Locate and identify every blood parasite.
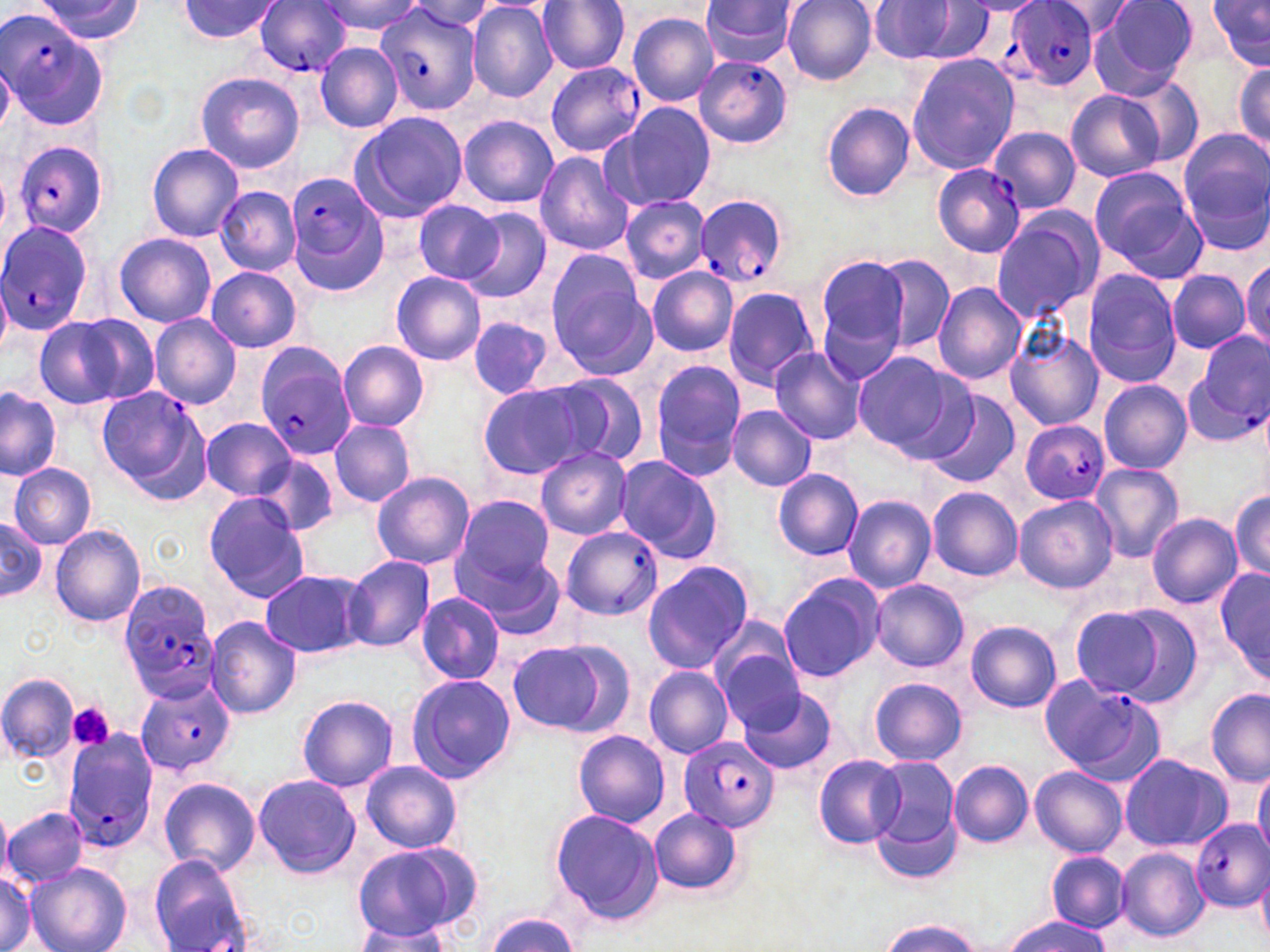

Approximate bounding boxes as (x1,y1)-(x2,y2) corner pairs in pixels.
Plasmodium falciparum-infected red blood cells (subset): (1010,0)-(1100,91), (253,2)-(353,76), (374,4)-(482,116), (0,8)-(103,130), (694,55)-(792,148), (545,61)-(644,156), (13,140)-(107,239), (933,163)-(1026,258), (285,172)-(387,288), (692,191)-(788,290), (0,217)-(95,336), (1194,333)-(1270,427), (257,352)-(359,461), (96,386)-(206,494), (1018,421)-(1109,504), (558,525)-(663,621), (1040,675)-(1163,780), (135,681)-(230,775), (62,731)-(159,854), (679,735)-(779,833), (1190,821)-(1270,912).
No Plasmodium ovale, Plasmodium malariae, Plasmodium vivax, Babesia divergens, or Trypanosoma brucei observed.

Summary:
  - Uninfected red blood cell locations (subset): (320,0)-(421,38), (700,0)-(801,65), (782,0)-(878,85), (1091,0)-(1198,94), (1209,0)-(1270,70), (35,1)-(142,44), (176,1)-(281,44), (405,1)-(499,35), (536,1)-(629,74), (1045,1)-(1139,38), (870,2)-(991,64), (468,3)-(559,102), (627,11)-(720,105), (314,42)-(404,132), (906,54)-(1020,175), (1232,54)-(1270,157), (0,60)-(14,138), (194,72)-(305,173), (1119,77)-(1203,164), (1065,89)-(1166,182), (821,101)-(915,201), (607,103)-(716,211), (348,111)-(468,224), (458,116)-(559,208), (987,126)-(1082,215), (1178,129)-(1270,236), (147,143)-(244,243), (533,151)-(633,256), (1087,165)-(1200,271), (216,187)-(300,277), (619,195)-(709,284), (412,199)-(504,285), (459,207)-(553,304), (990,213)-(1102,322), (114,232)-(216,327), (544,249)-(647,362), (814,252)-(912,359), (873,253)-(955,353), (1241,259)-(1270,354), (206,266)-(302,354), (646,267)-(736,355), (1166,270)-(1251,353), (390,271)-(486,366), (1082,272)-(1181,387), (0,281)-(11,359), (931,282)-(1026,385), (723,286)-(820,391), (32,313)-(148,410), (150,314)-(242,408), (468,319)-(555,400), (1003,328)-(1105,432), (338,341)-(430,432), (769,344)-(865,445), (852,353)-(962,452), (649,362)-(750,478), (536,373)-(650,468), (1099,380)-(1192,472), (477,383)-(592,480), (0,386)-(61,480), (922,393)-(1020,488), (727,405)-(816,491), (202,418)-(295,499), (329,420)-(415,507), (536,447)-(632,539), (251,454)-(339,538), (609,454)-(722,564), (1089,461)-(1183,563), (9,464)-(96,548), (772,469)-(864,561), (372,472)-(475,570), (927,488)-(1022,581), (1231,490)-(1270,581), (204,492)-(312,602), (453,494)-(555,589), (841,495)-(936,594), (1014,495)-(1118,594), (1146,513)-(1242,608), (0,515)-(47,605), (50,523)-(147,628), (451,538)-(566,635), (343,555)-(434,655), (641,560)-(754,674), (1216,565)-(1269,682), (260,568)-(370,658), (777,574)-(886,682), (870,579)-(969,673), (417,593)-(504,684), (1068,603)-(1188,704), (205,617)-(301,719), (966,622)-(1064,713), (506,638)-(624,735), (716,645)-(809,734), (643,664)-(732,759), (0,672)-(79,762), (406,675)-(515,782), (869,677)-(965,766), (740,687)-(839,775), (1205,690)-(1269,785), (297,693)-(399,792), (573,730)-(670,827), (864,753)-(961,872), (1119,753)-(1232,852), (813,755)-(906,848), (948,759)-(1035,847), (360,760)-(462,853), (1253,765)-(1270,860), (1031,766)-(1127,859), (253,774)-(360,878), (158,777)-(260,875), (0,807)-(13,885), (1,807)-(88,886), (548,808)-(664,925), (650,809)-(741,893), (353,847)-(468,945), (1117,848)-(1210,942), (1047,850)-(1129,932), (151,853)-(252,951), (28,864)-(131,952), (1257,867)-(1270,947), (0,871)-(36,952), (483,914)-(578,951), (1000,916)-(1115,951), (876,919)-(986,951), (352,927)-(454,952)
  - Platelet locations: (68,701)-(115,751)
  - Slide-level diagnosis: Plasmodium falciparum
  - Stain: May-Grünwald-Giemsa
  - Field of view: one of a larger specimen
  - Preparation: thin blood smear
  - Magnification: 1000x
  - Image size: 1270×952 pixels
  - Modality: light microscopy